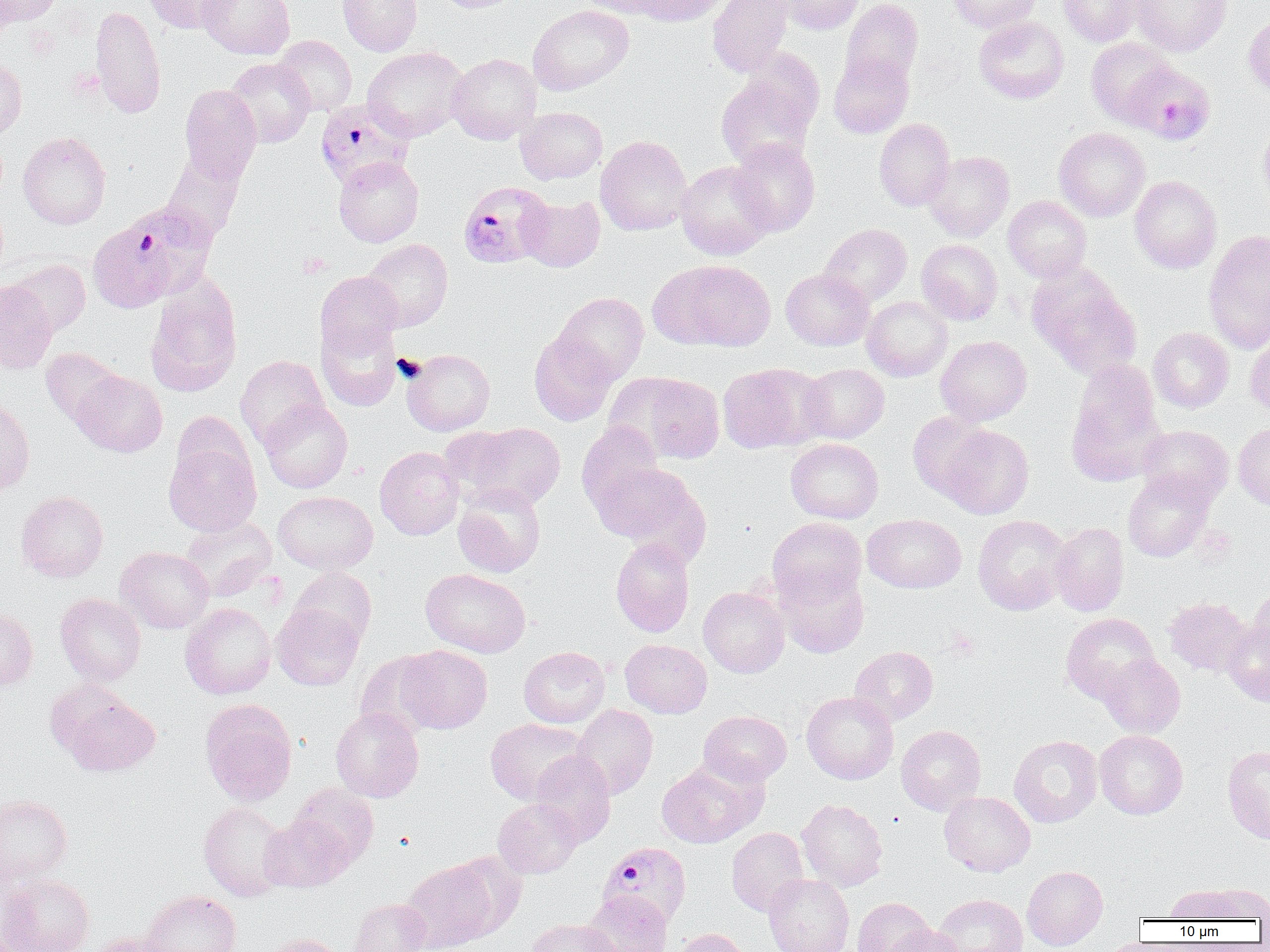

Summary:
  - Coordinate format: approximate bounding boxes as (x1,y1)-(x2,y2) corner pairs in pixels
  - Platelet locations: (299,252)-(332,278), (392,353)-(426,382), (946,630)-(979,660)
  - Uninfected red blood cell locations: (1,0)-(62,27), (143,0)-(236,33), (198,0)-(294,60), (338,0)-(422,56), (430,0)-(525,13), (577,0)-(666,17), (628,0)-(728,26), (708,0)-(792,77), (776,0)-(864,35), (841,0)-(923,85), (947,0)-(1040,33), (1058,0)-(1146,46), (1132,0)-(1232,56), (90,4)-(166,119), (528,5)-(634,95), (1244,13)-(1270,102), (974,16)-(1069,104), (274,35)-(357,115), (1086,37)-(1176,127), (363,47)-(468,141), (738,48)-(824,135), (828,52)-(914,138), (447,53)-(541,144), (0,55)-(27,138), (225,58)-(315,148), (716,74)-(818,170), (179,85)-(262,183), (516,106)-(607,184), (874,119)-(955,211), (1257,119)-(1270,209), (1054,127)-(1150,221), (18,131)-(111,229), (595,135)-(693,236), (729,138)-(820,237), (924,151)-(1014,241), (161,152)-(244,243), (334,156)-(423,247), (676,162)-(773,259), (1129,175)-(1222,273), (519,195)-(605,272), (1003,195)-(1091,282), (820,223)-(912,306), (1203,229)-(1270,351), (362,239)-(452,331), (916,239)-(1003,325), (6,259)-(91,336), (652,260)-(775,351), (1027,266)-(1142,378), (781,269)-(874,351), (315,271)-(403,360), (145,275)-(243,397), (0,280)-(57,374), (553,292)-(648,384), (862,296)-(952,381), (317,320)-(402,411), (1148,327)-(1234,412), (1245,329)-(1270,417), (529,331)-(618,426), (936,336)-(1031,425), (40,348)-(124,426), (402,348)-(495,436), (235,355)-(329,448), (717,363)-(825,454), (800,363)-(889,443), (1067,363)-(1165,484), (71,370)-(167,457), (628,374)-(726,464), (0,394)-(35,496), (259,400)-(353,493), (908,411)-(990,500), (577,422)-(665,513), (459,423)-(566,510), (1233,423)-(1270,510), (1138,424)-(1234,505), (940,425)-(1034,519), (785,438)-(883,523), (164,442)-(261,536), (374,446)-(464,540), (591,461)-(702,552), (1122,469)-(1215,562), (453,483)-(546,578), (16,490)-(109,582), (273,491)-(378,574), (862,514)-(966,593), (972,514)-(1073,615), (179,515)-(277,599), (767,517)-(866,606), (1049,522)-(1129,616), (611,537)-(695,637), (116,547)-(214,633), (288,567)-(377,649), (776,567)-(869,658), (421,568)-(531,658), (698,586)-(790,677), (1247,588)-(1270,666), (55,593)-(146,685), (1164,596)-(1253,676), (180,603)-(276,699), (271,603)-(363,691), (0,605)-(37,692), (1060,613)-(1161,704), (1221,619)-(1270,707), (620,639)-(712,717), (397,645)-(492,734), (519,646)-(610,727), (849,646)-(938,725), (355,651)-(443,738), (1098,654)-(1185,737), (801,691)-(898,784), (60,692)-(160,776), (200,699)-(298,805), (571,704)-(658,799), (330,708)-(424,802), (699,710)-(792,786), (485,718)-(589,805), (896,725)-(985,815), (1094,730)-(1188,819), (1009,735)-(1103,827), (1222,744)-(1270,845), (529,751)-(616,846), (656,758)-(763,848), (289,784)-(378,868), (939,791)-(1035,877), (0,794)-(72,885), (493,798)-(582,878), (796,799)-(888,892), (198,802)-(291,901), (259,815)-(352,892), (726,827)-(809,916), (447,851)-(529,936), (401,859)-(499,952), (1022,865)-(1108,950), (1,873)-(95,952), (763,874)-(854,952), (1202,883)-(1270,921), (1166,884)-(1249,922), (141,890)-(242,952), (582,891)-(672,952), (932,893)-(1028,952), (853,897)-(933,952), (348,898)-(431,952), (525,918)-(619,952), (884,924)-(964,952), (672,928)-(752,952), (88,932)-(181,952), (263,933)-(346,952)
  - Plasmodium falciparum-infected red blood cell locations: (1125,62)-(1215,145), (316,100)-(416,187), (457,181)-(554,269), (88,202)-(217,312), (598,841)-(691,927)
  - Slide-level diagnosis: Plasmodium falciparum
  - Magnification: 1000x
  - Preparation: thin blood smear
  - Field of view: single
  - Modality: light microscopy
  - Image size: 1270×952 pixels